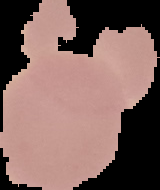
malaria status = uninfected
preparation = thin blood smear
image type = cell region segmented out of the field of view; surrounding area masked to black
image size = 160×190 pixels